Outline each blood parasite and name the species.
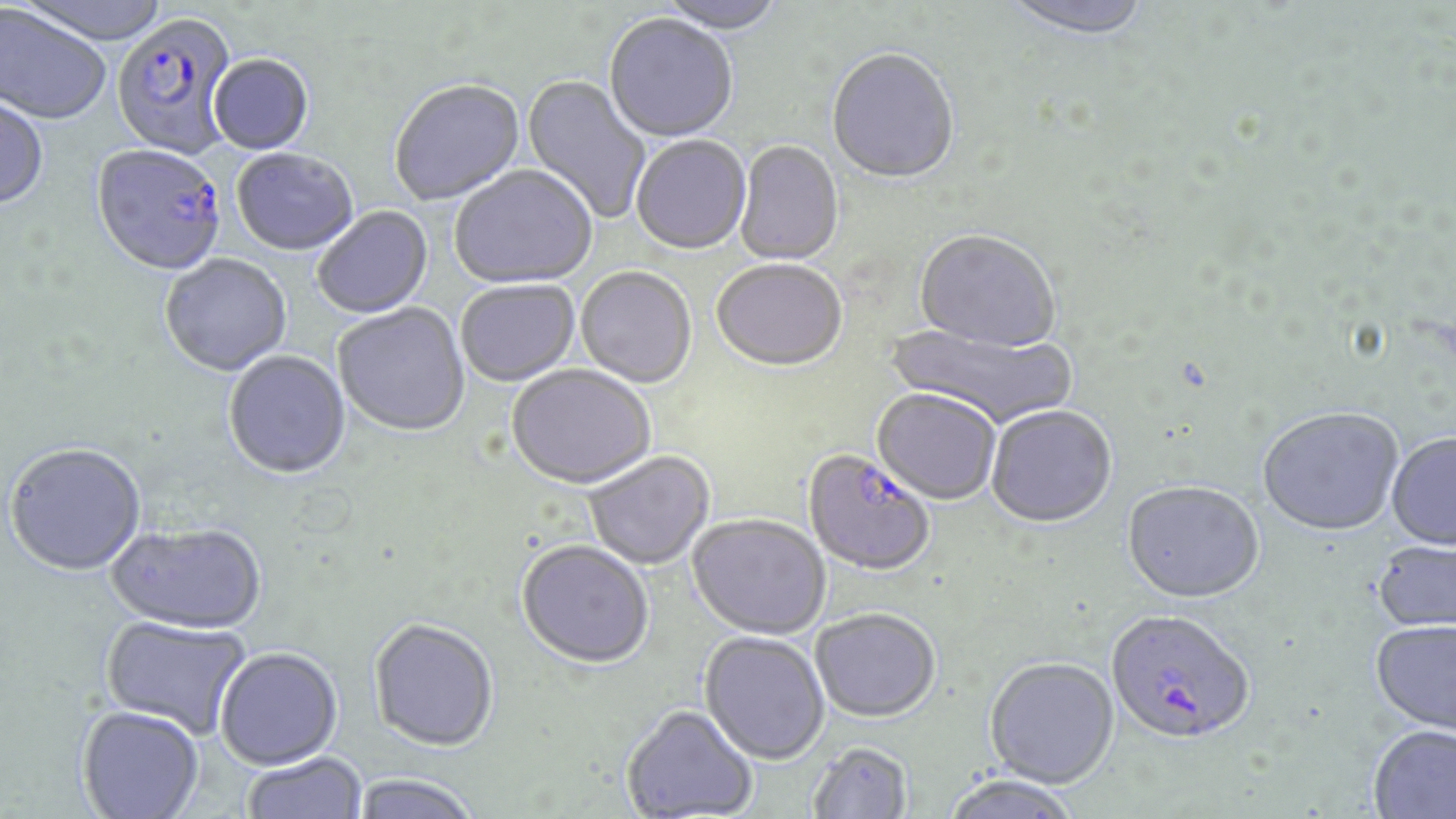
Approximate bounding boxes as [x1, y1, x2, y2] in pixels.
Plasmodium falciparum-infected red blood cells: [111, 15, 241, 162], [91, 146, 226, 279], [804, 451, 934, 577], [1105, 609, 1254, 746].
No Plasmodium ovale, Plasmodium malariae, Plasmodium vivax, Babesia divergens, or Trypanosoma brucei observed.

Summary:
  - Uninfected red blood cell locations: [12, 0, 176, 48], [652, 0, 788, 35], [999, 0, 1155, 43], [0, 5, 111, 127], [603, 15, 739, 144], [826, 51, 960, 186], [209, 56, 314, 156], [519, 75, 652, 224], [389, 80, 527, 207], [0, 95, 50, 211], [631, 137, 751, 256], [734, 142, 843, 267], [232, 151, 359, 256], [449, 167, 598, 290], [312, 207, 434, 319], [914, 231, 1060, 354], [159, 256, 292, 378], [711, 261, 847, 374], [576, 268, 697, 389], [457, 281, 580, 387], [334, 304, 471, 438], [884, 322, 1080, 431], [223, 352, 351, 481], [506, 366, 656, 491], [872, 390, 1001, 505], [987, 406, 1117, 530], [1258, 410, 1403, 538], [1386, 433, 1456, 551], [4, 444, 147, 577], [584, 451, 715, 570], [1122, 482, 1264, 605], [688, 514, 830, 639], [106, 523, 266, 634], [516, 540, 654, 669], [1372, 541, 1456, 635], [811, 607, 941, 722], [100, 615, 251, 738], [368, 618, 499, 751], [1370, 621, 1456, 737], [699, 630, 830, 764], [216, 647, 343, 769], [984, 657, 1120, 789], [621, 704, 758, 819], [77, 705, 204, 818], [1367, 726, 1456, 819], [807, 742, 913, 819], [242, 752, 367, 819], [350, 774, 481, 819], [939, 775, 1084, 819]
  - Slide-level diagnosis: Plasmodium falciparum
  - Stain: May-Grünwald-Giemsa
  - Image size: 1456×819 pixels
  - Field of view: single
  - Preparation: thin blood film
  - Modality: light microscopy
  - Magnification: 1000x